Assess the morphology of the red blood cells.
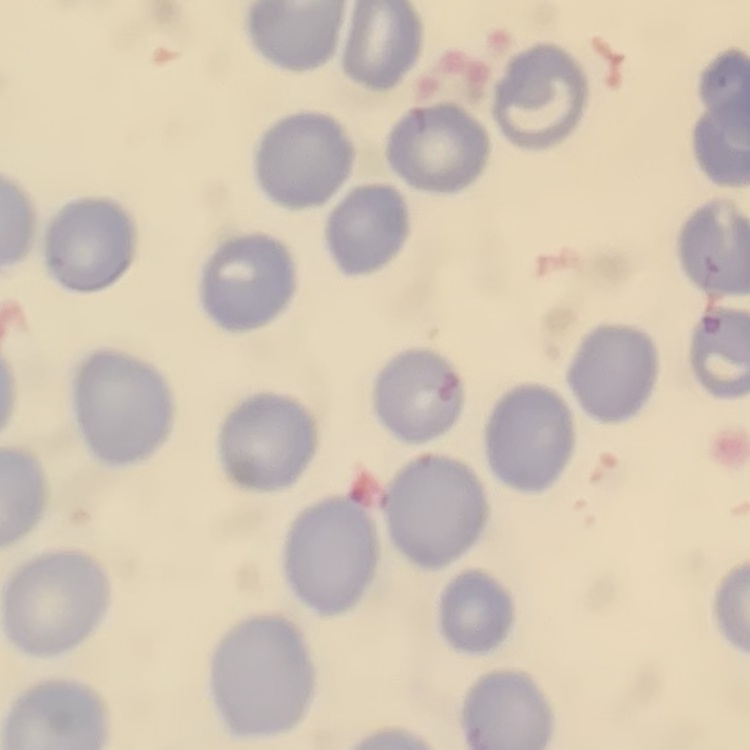
No rouleaux formation.

Summary:
  - Preparation: thin peripheral smear
  - Image type: square crop of a larger photomicrograph
  - Stain: Field's or Giemsa